Name the parasite shown.
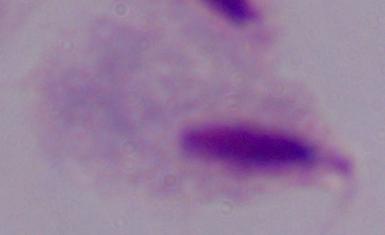
This is a trichomonad.

1000x magnification. Micrograph.